Assess the morphology of the red blood cells.
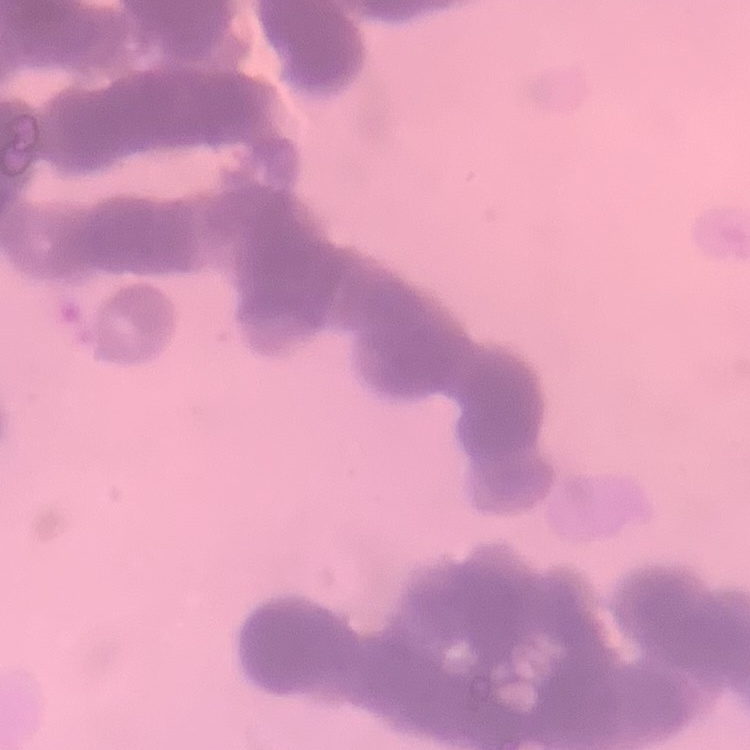

Rouleaux formation.

Thin blood film. One tile cut from a larger photomicrograph. Stained with either Field's or Giemsa.